Assess this cell for malaria.
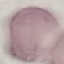

Uninfected.

Giemsa-stained preparation. Thin blood film. Cell patch, automatically extracted from a larger field of view and resized to 64 × 64 pixels. Photographed with a smartphone camera at the microscope eyepiece.